Outline every parasitised red blood cell.
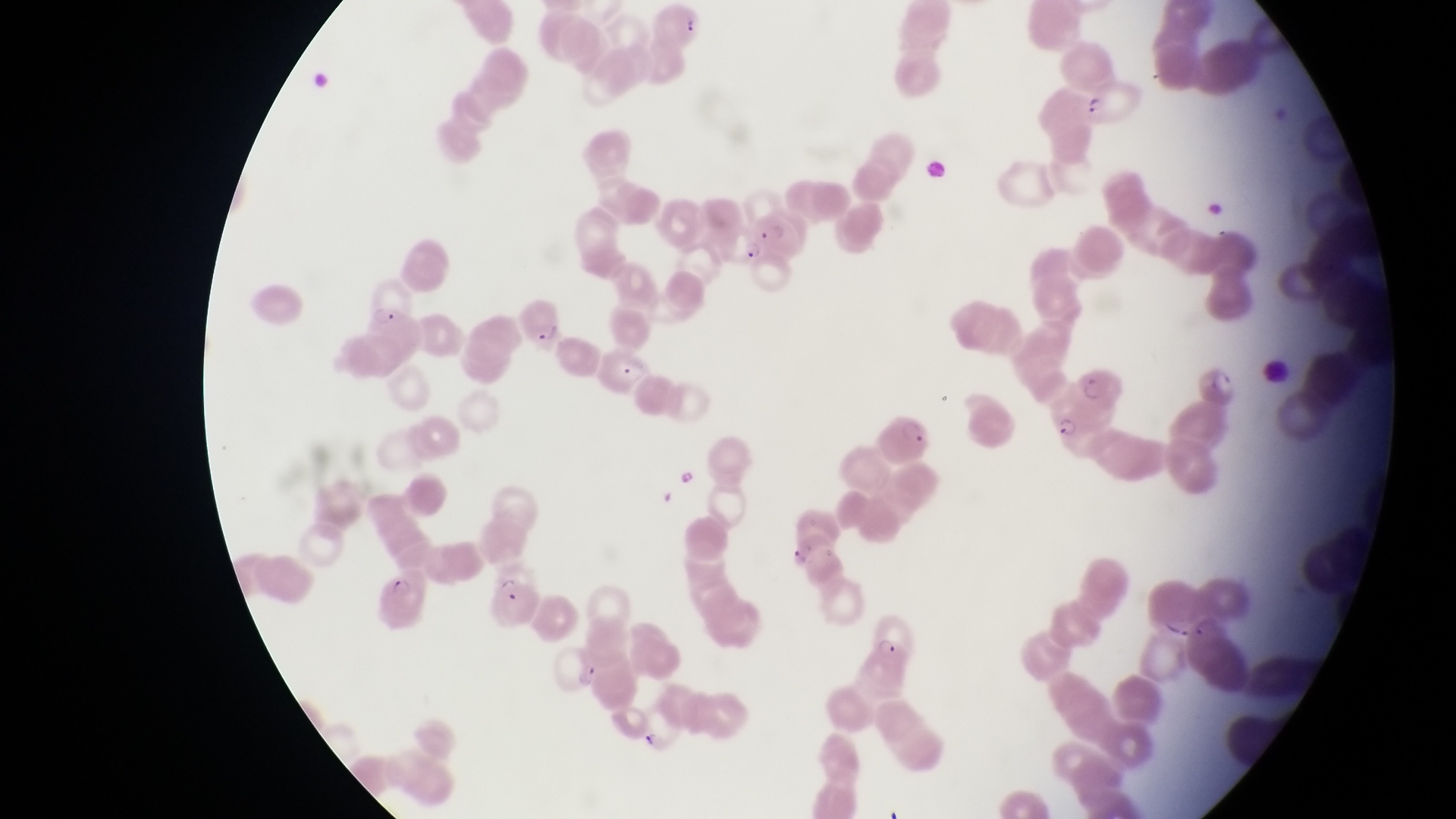
Approximate bounding boxes as (left, top, right, bottom) in pixels.
Parasitised red blood cells: (651, 2, 703, 48), (1084, 79, 1147, 125), (732, 202, 801, 265), (363, 278, 408, 331), (519, 297, 562, 355), (595, 351, 650, 396), (1195, 351, 1244, 406), (1075, 362, 1125, 411), (1047, 394, 1113, 437), (488, 570, 540, 631), (375, 571, 433, 631), (864, 608, 919, 664), (1189, 613, 1249, 687).

trophozoite_locations: 'approximate bounding boxes as (left, top, right, bottom) in pixels: (576, 663, 600, 690)'
image_size: 1456×819 pixels
country: Uganda
capture: smartphone photograph through the eyepiece of an Olympus CX-23 microscope
magnification: 1000x
field_of_view: single
preparation: thin blood film